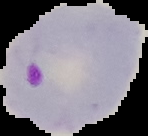

The area outside the segmented cell region is set to black. Malaria status: parasitized. Image is 148×136 pixels. From a thin blood smear.